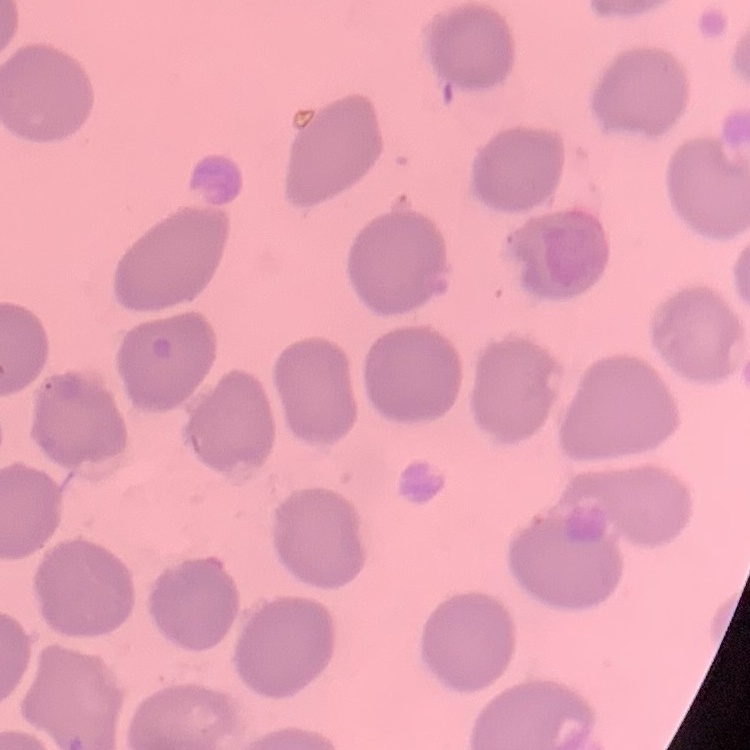

Summary:
  - Erythrocyte morphology: no rouleaux formation
  - Preparation: thin blood smear
  - Stain: Field's or Giemsa
  - Image type: square crop of a larger photomicrograph